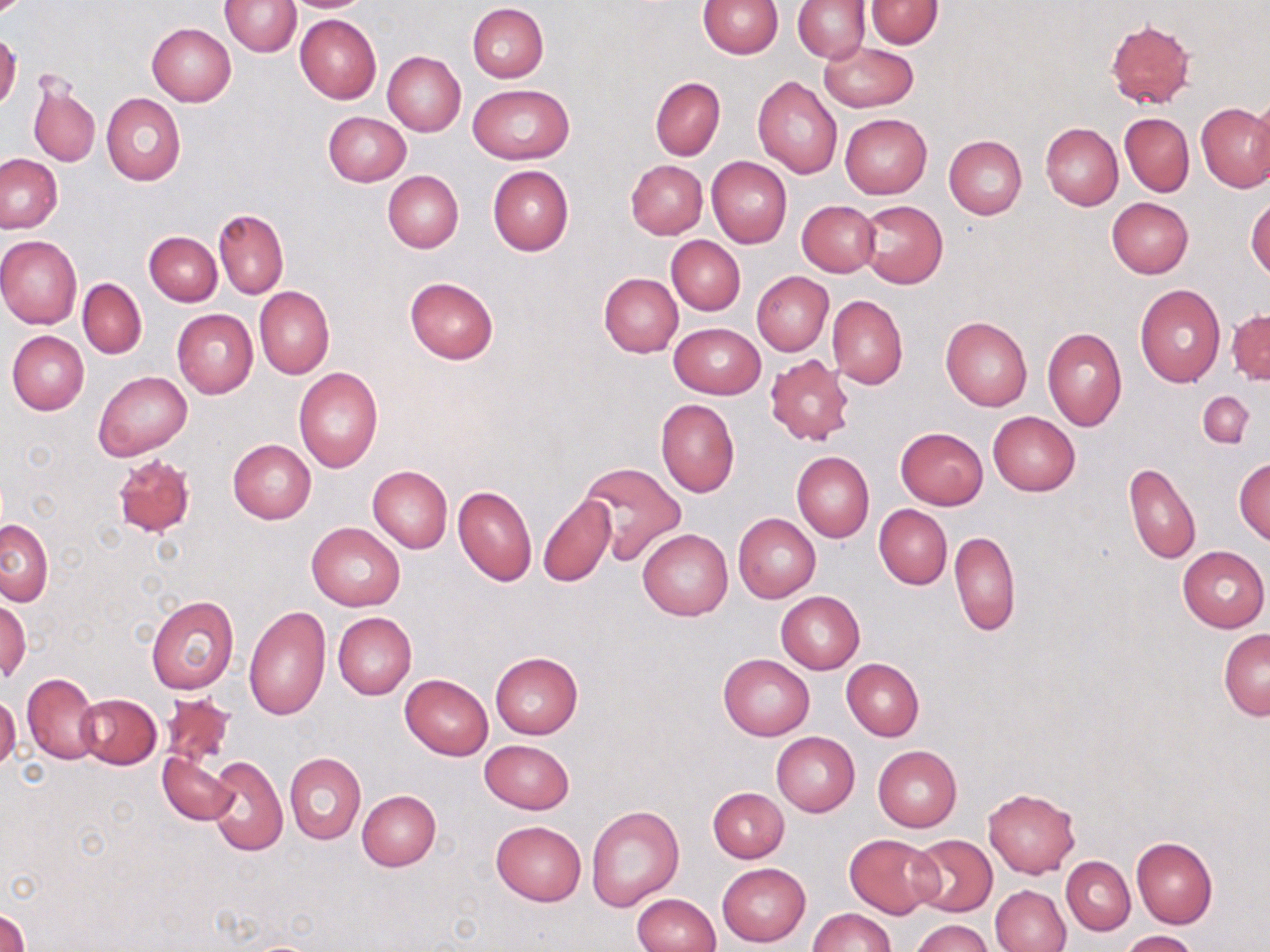 Approximate bounding boxes as (x1,y1)-(x2,y2) corner pairs in pixels. Uninfected red blood cell locations: (280,0)-(373,12), (698,0)-(782,58), (792,0)-(870,63), (865,0)-(944,48), (222,1)-(300,56), (467,4)-(548,82), (295,14)-(381,104), (1105,19)-(1196,108), (147,22)-(235,107), (0,33)-(21,109), (819,41)-(918,111), (382,52)-(465,135), (752,76)-(843,180), (29,77)-(99,168), (650,77)-(724,160), (469,84)-(571,164), (101,93)-(186,185), (1249,94)-(1270,190), (1197,102)-(1270,193), (323,112)-(411,186), (1120,112)-(1194,196), (840,114)-(932,198), (1040,122)-(1123,210), (944,136)-(1027,219), (1,154)-(63,233), (707,157)-(792,247), (626,160)-(708,239), (487,165)-(572,256), (384,171)-(463,252), (1106,197)-(1193,279), (1247,197)-(1270,279), (797,200)-(880,277), (856,200)-(947,287), (214,208)-(288,299), (144,232)-(222,306), (666,235)-(745,315), (0,236)-(82,328), (751,271)-(833,356), (598,273)-(682,357), (404,277)-(498,364), (77,278)-(146,357), (1134,285)-(1225,387), (255,287)-(335,379), (827,294)-(908,389), (172,309)-(258,398), (1228,309)-(1269,385), (940,316)-(1032,410), (669,323)-(765,398), (1043,327)-(1127,431), (8,331)-(89,415), (765,354)-(854,445), (294,368)-(383,472), (95,371)-(192,460), (1198,391)-(1254,449), (655,398)-(739,497), (988,411)-(1080,496), (895,427)-(988,509), (228,439)-(316,523), (792,451)-(874,542), (1234,457)-(1270,545), (581,462)-(686,564), (1125,462)-(1200,564), (367,465)-(452,553), (453,484)-(537,586), (538,493)-(616,586), (874,504)-(952,589), (734,513)-(821,602), (1,518)-(53,605), (307,522)-(405,611), (638,528)-(733,621), (950,530)-(1019,636), (1178,546)-(1269,631), (775,590)-(865,673), (146,595)-(239,694), (0,600)-(29,681), (243,605)-(330,720), (333,612)-(416,699), (1218,628)-(1269,719), (489,652)-(583,738), (718,654)-(814,739), (841,658)-(924,742), (22,672)-(101,765), (400,674)-(493,760), (0,693)-(21,773), (159,693)-(234,767), (74,694)-(162,768), (771,731)-(860,816), (480,740)-(574,814), (873,746)-(962,831), (158,752)-(237,825), (285,752)-(366,844), (204,754)-(288,856), (709,787)-(789,862), (983,787)-(1080,878), (356,789)-(441,870), (586,805)-(684,912), (491,821)-(586,905), (845,834)-(939,918), (907,834)-(997,916), (1131,838)-(1217,928), (1062,856)-(1135,934), (717,863)-(810,946), (990,884)-(1071,952), (632,893)-(721,952), (0,908)-(27,952), (809,908)-(896,952), (912,918)-(995,952), (1122,930)-(1200,952). Slide-level diagnosis: negative for blood parasites. Thin blood smear. May-Grünwald-Giemsa stain. Captured at 1000x magnification. Image is 1270×952 pixels. Optical microscopy. Single field of view.